Evaluate for malaria.
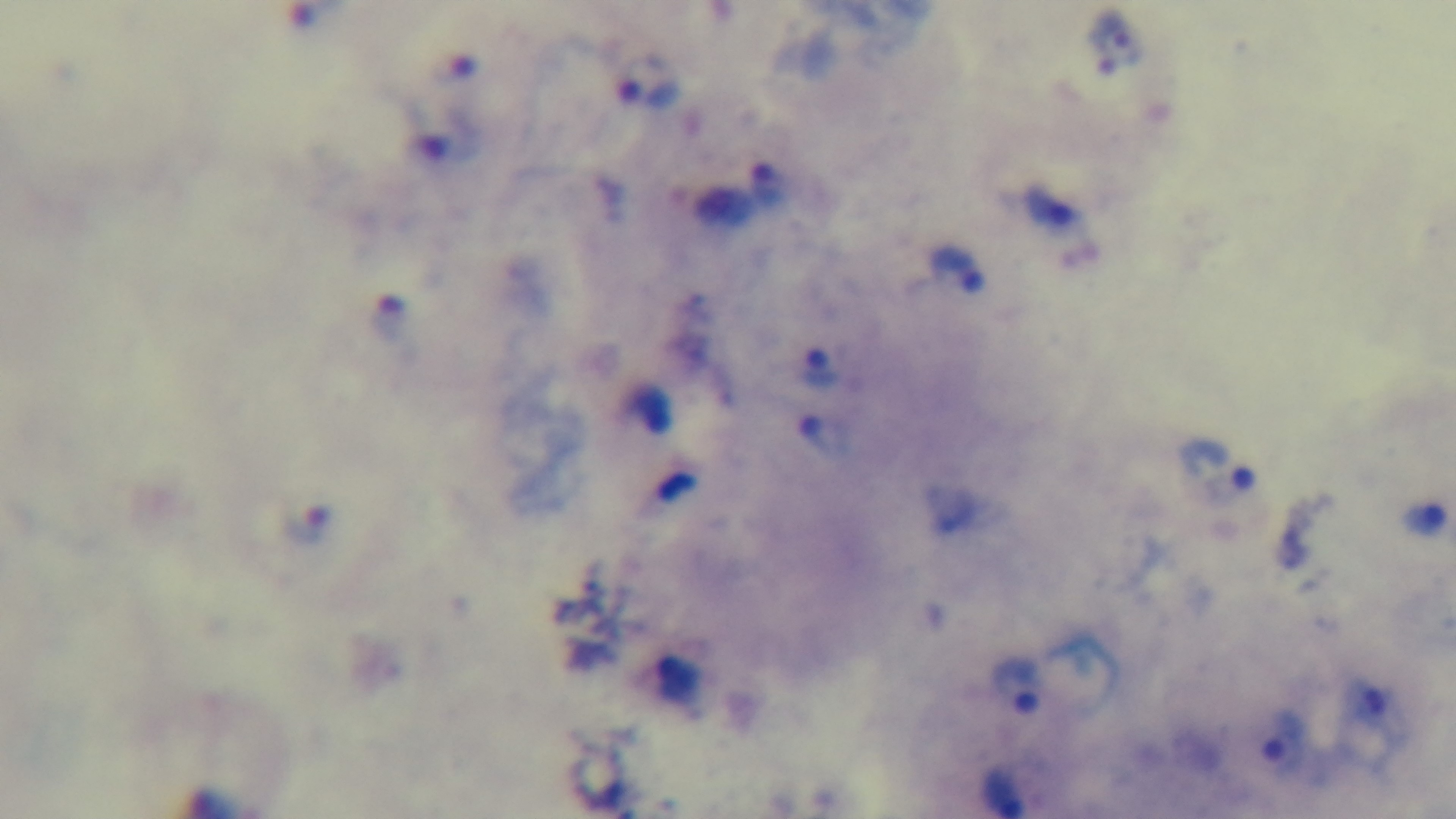

It is infected.

Giemsa-stained. Preparation: thick smear. Single field of view. 100x oil-immersion objective. Mounted 4K digital camera. Photomicrograph.